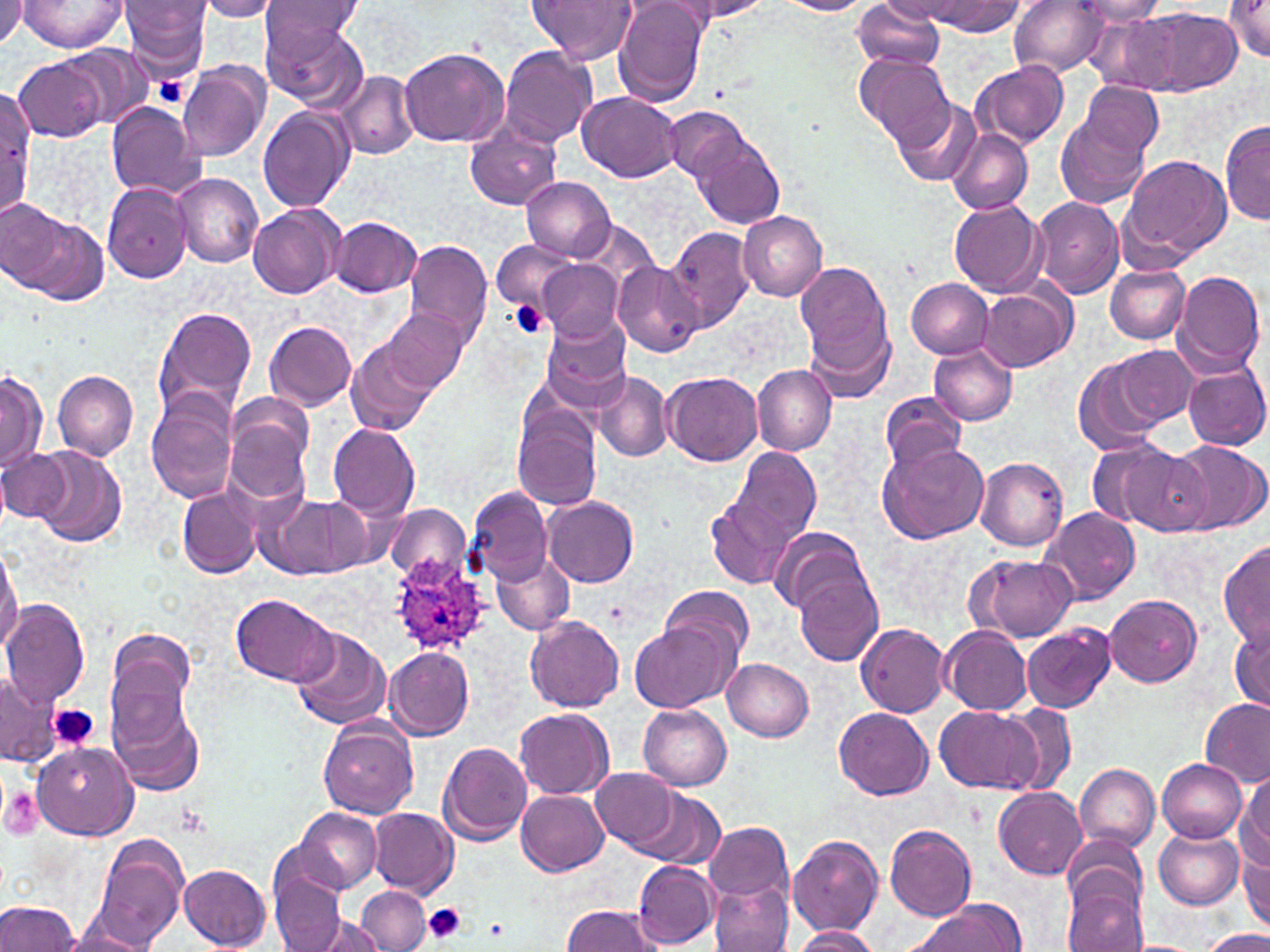 Approximate bounding boxes as (x1,y1)-(x2,y2) corner pairs in pixels. Plasmodium ovale-infected red blood cell locations: (386,558)-(490,655). Uninfected red blood cell locations: (0,0)-(28,50), (121,0)-(214,77), (195,0)-(283,20), (527,0)-(637,65), (669,0)-(773,22), (851,0)-(949,73), (928,0)-(1025,35), (1009,0)-(1109,75), (1072,0)-(1170,25), (1225,0)-(1270,59), (17,1)-(128,54), (259,1)-(364,53), (613,1)-(708,107), (775,1)-(871,15), (883,2)-(973,22), (1143,8)-(1239,93), (261,13)-(368,110), (59,44)-(153,129), (399,47)-(509,146), (500,47)-(597,150), (854,54)-(955,151), (12,57)-(105,143), (178,60)-(271,163), (971,62)-(1070,150), (337,72)-(419,160), (1077,80)-(1163,162), (578,91)-(682,182), (0,92)-(31,214), (892,96)-(982,186), (1056,100)-(1154,210), (104,101)-(203,197), (257,105)-(355,212), (665,107)-(748,185), (1220,116)-(1269,226), (465,122)-(563,212), (946,127)-(1032,214), (692,131)-(785,229), (1121,153)-(1232,260), (170,174)-(263,267), (521,177)-(615,261), (102,181)-(194,284), (1030,197)-(1123,298), (948,199)-(1046,297), (2,200)-(79,293), (248,202)-(344,297), (738,210)-(828,301), (330,217)-(422,297), (666,227)-(756,334), (404,238)-(494,349), (492,241)-(576,313), (538,259)-(624,342), (795,260)-(892,368), (612,263)-(704,356), (1105,264)-(1190,343), (1172,270)-(1266,378), (907,279)-(993,357), (977,287)-(1073,371), (153,307)-(256,421), (380,308)-(469,394), (540,313)-(632,408), (804,317)-(893,406), (265,321)-(356,411), (346,337)-(438,437), (929,345)-(1017,425), (1104,347)-(1198,430), (1073,350)-(1173,454), (1182,363)-(1269,450), (751,364)-(838,453), (53,369)-(138,461), (0,370)-(46,477), (593,371)-(673,462), (662,371)-(763,466), (880,391)-(966,475), (145,398)-(238,505), (224,405)-(313,508), (511,408)-(602,511), (328,424)-(420,519), (1169,440)-(1268,535), (876,442)-(988,544), (1119,445)-(1215,535), (32,447)-(126,548), (721,448)-(821,559), (0,449)-(71,523), (975,456)-(1068,550), (469,486)-(551,585), (177,487)-(260,578), (705,495)-(798,593), (544,496)-(638,586), (267,497)-(371,580), (385,505)-(471,585), (1040,508)-(1141,605), (770,529)-(872,615), (1217,540)-(1270,650), (0,546)-(21,657), (492,553)-(575,633), (966,553)-(1078,642), (794,570)-(883,667), (661,584)-(754,664), (231,594)-(337,687), (1104,594)-(1203,688), (1,600)-(89,705), (524,616)-(624,712), (1230,617)-(1270,714), (856,622)-(951,717), (1022,622)-(1116,713), (631,623)-(733,712), (291,627)-(389,730), (939,628)-(1032,715), (105,629)-(198,738), (384,647)-(475,739), (722,659)-(814,740), (0,670)-(59,766), (109,688)-(205,797), (1199,697)-(1270,786), (1001,704)-(1078,794), (638,705)-(731,790), (933,706)-(1039,793), (835,707)-(933,799), (515,709)-(613,799), (319,720)-(419,819), (438,743)-(532,845), (32,744)-(138,838), (1156,759)-(1247,841), (1074,764)-(1159,851), (592,766)-(682,853), (1237,774)-(1269,873), (995,787)-(1086,879), (517,789)-(609,876), (630,789)-(725,870), (368,807)-(459,896), (294,808)-(380,895), (706,822)-(795,904), (884,824)-(976,922), (1153,826)-(1245,910), (93,835)-(189,951), (787,835)-(884,935), (1062,835)-(1147,916), (1240,847)-(1270,932), (633,861)-(719,949), (179,864)-(272,950), (270,873)-(347,952), (710,877)-(794,952), (1061,880)-(1148,952), (357,886)-(431,951), (0,899)-(81,951), (562,904)-(663,952), (903,904)-(1022,951), (308,914)-(384,952), (788,926)-(882,952), (1200,928)-(1270,951), (57,930)-(155,951), (1130,940)-(1197,952). Platelet locations: (153,74)-(190,108), (509,299)-(550,340), (50,703)-(100,751), (1,786)-(44,837), (421,903)-(469,943), (484,917)-(509,941). Slide-level diagnosis: Plasmodium ovale. Image is 1270×952 pixels. Captured at 1000x magnification. May-Grünwald-Giemsa-stained preparation. Thin blood smear. Optical microscopy. One field of a larger specimen.